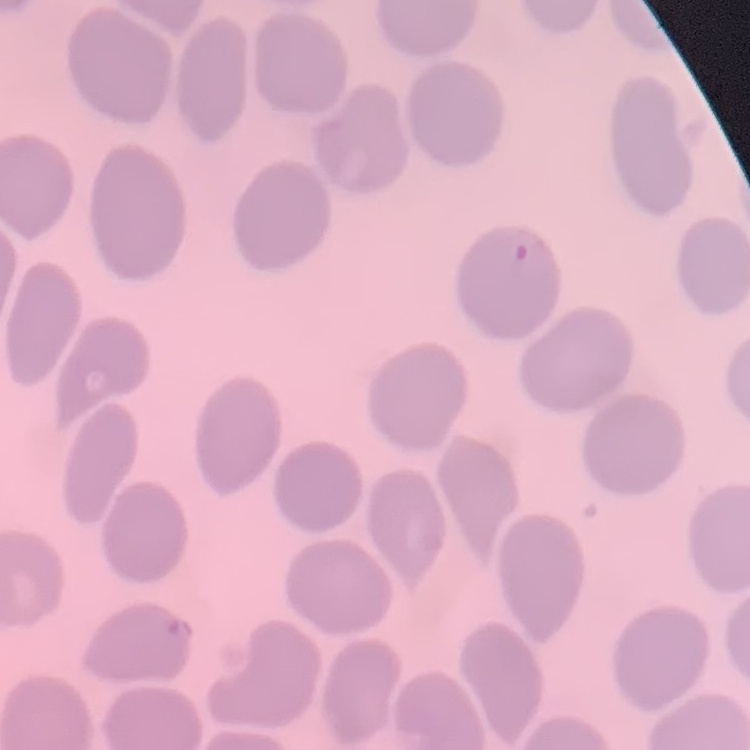

Summary:
  - Erythrocyte morphology: no rouleaux formation
  - Stain: Field's or Giemsa
  - Preparation: thin blood smear
  - Image type: square crop of a larger photomicrograph